Identify the blood parasite species.
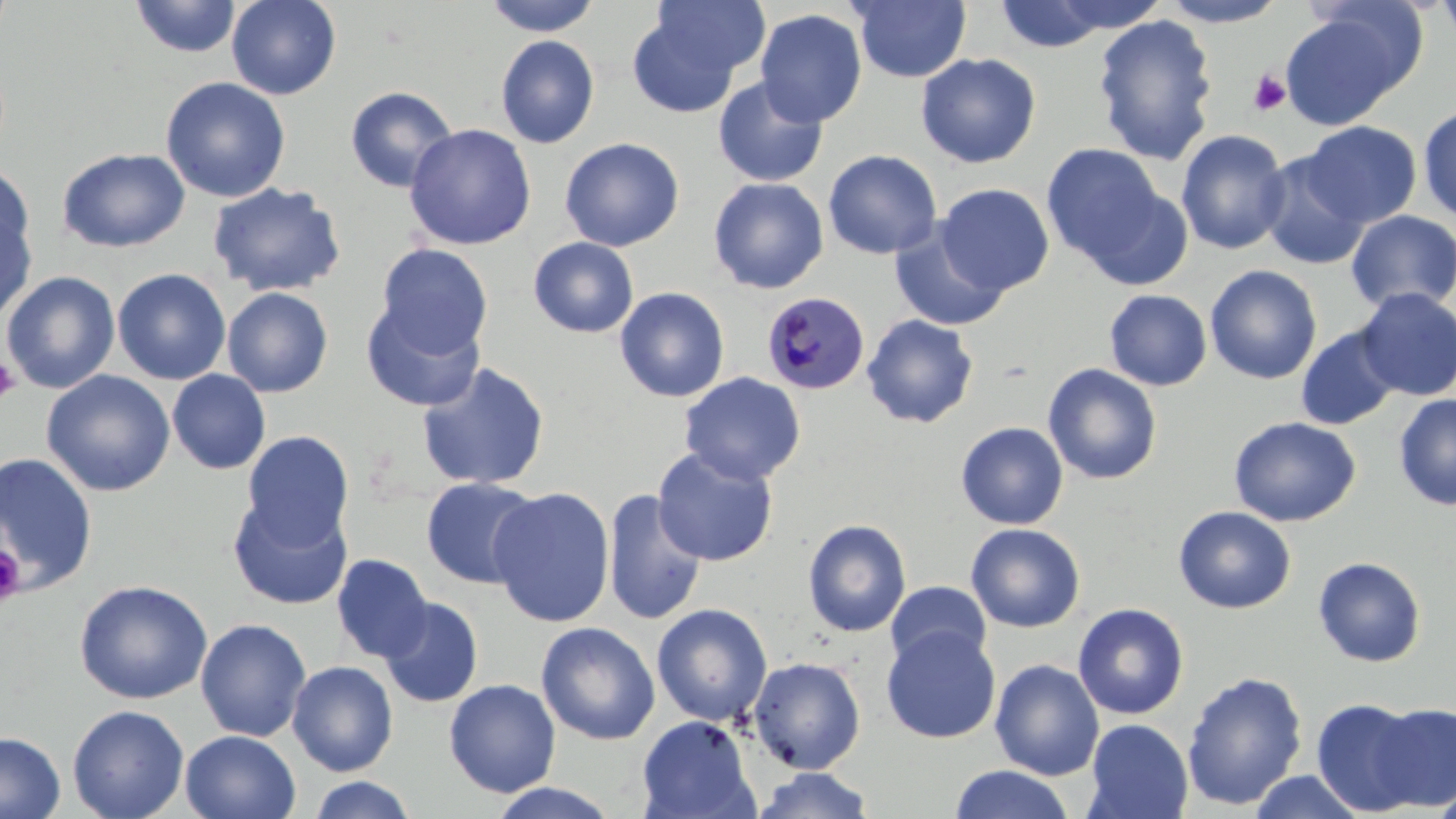

Plasmodium malariae.

Summary:
  - Coordinate format: approximate bounding boxes as (x1,y1)-(x2,y2) corner pairs in pixels
  - Uninfected red blood cell locations: (129,0)-(242,59), (226,0)-(342,100), (483,0)-(602,37), (648,0)-(770,81), (1043,0)-(1172,35), (1158,0)-(1289,27), (1434,0)-(1456,49), (851,1)-(972,83), (992,1)-(1116,53), (754,9)-(868,128), (1279,9)-(1415,130), (627,10)-(744,118), (1092,14)-(1219,165), (495,34)-(600,149), (916,53)-(1041,168), (160,76)-(291,202), (712,77)-(828,187), (345,85)-(459,193), (1418,104)-(1456,224), (1300,121)-(1422,227), (404,123)-(537,250), (1175,129)-(1290,255), (559,137)-(684,251), (1041,144)-(1166,265), (57,147)-(191,253), (823,149)-(942,260), (1258,152)-(1371,271), (0,161)-(34,266), (708,177)-(829,294), (208,182)-(346,297), (1082,183)-(1194,290), (936,184)-(1055,295), (0,203)-(37,323), (1345,210)-(1456,315), (890,222)-(1011,332), (528,236)-(639,338), (376,243)-(493,357), (1205,264)-(1322,384), (112,268)-(231,385), (1,270)-(120,394), (221,287)-(334,398), (614,287)-(729,402), (1354,287)-(1456,401), (1104,288)-(1212,391), (362,302)-(485,411), (862,314)-(979,428), (1295,324)-(1402,431), (417,361)-(550,491), (1043,363)-(1163,485), (167,369)-(271,475), (41,370)-(176,497), (679,371)-(806,485), (1393,393)-(1456,510), (1228,416)-(1361,527), (955,421)-(1069,530), (242,430)-(354,545), (651,447)-(779,566), (0,452)-(98,593), (420,476)-(542,589), (488,487)-(615,627), (602,488)-(707,626), (227,494)-(352,610), (1174,506)-(1296,614), (802,518)-(912,637), (965,523)-(1085,633), (331,553)-(433,662), (1313,556)-(1427,667), (74,579)-(213,704), (886,581)-(991,670), (378,596)-(484,708), (1072,602)-(1190,719), (651,603)-(772,726), (194,618)-(312,742), (536,621)-(660,745), (881,626)-(1001,744), (747,657)-(866,774), (989,659)-(1105,780), (288,660)-(398,776), (1181,670)-(1308,810), (443,678)-(561,797), (1311,697)-(1428,815), (1369,702)-(1456,811), (67,704)-(190,819), (636,715)-(759,819), (1084,718)-(1193,819), (180,730)-(301,818), (0,731)-(65,819), (948,765)-(1076,819), (752,767)-(876,819), (1246,770)-(1369,818), (306,775)-(419,819), (487,782)-(620,818), (1430,782)-(1456,819)
  - Plasmodium malariae-infected red blood cell locations: (760,290)-(870,396)
  - Platelet locations: (1248,69)-(1291,116), (0,355)-(21,404), (0,543)-(26,606)
  - Modality: optical microscopy
  - Image size: 1456×819 pixels
  - Field of view: one of a larger specimen
  - Magnification: 1000x
  - Stain: May-Grünwald-Giemsa
  - Preparation: thin blood smear